Report the malaria status of this cell.
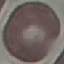
Uninfected.

Summary:
  - Capture: smartphone through the microscope eyepiece
  - Stain: Giemsa
  - Image type: automatically extracted cell patch, resized to 64 × 64 pixels
  - Preparation: thin smear